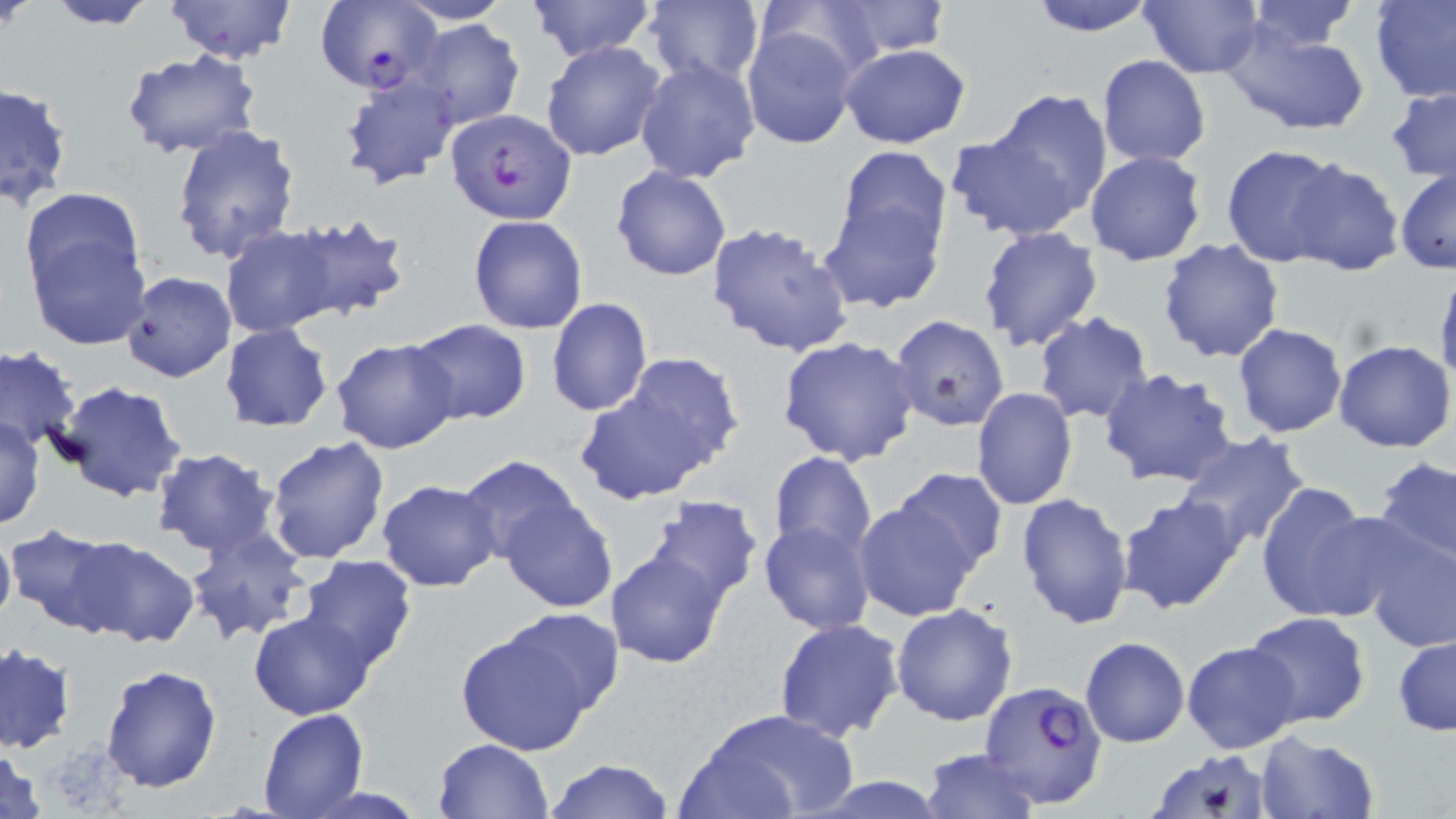 Approximate bounding boxes as named x1/y1/x2/y2 corners in pixels. Uninfected red blood cell locations: (x1=163, y1=0, x2=296, y2=64), (x1=526, y1=0, x2=657, y2=64), (x1=755, y1=0, x2=888, y2=83), (x1=1027, y1=0, x2=1159, y2=37), (x1=1136, y1=0, x2=1263, y2=78), (x1=1369, y1=0, x2=1456, y2=103), (x1=41, y1=1, x2=159, y2=29), (x1=394, y1=1, x2=514, y2=24), (x1=642, y1=1, x2=764, y2=85), (x1=825, y1=1, x2=952, y2=58), (x1=1244, y1=1, x2=1363, y2=53), (x1=406, y1=18, x2=526, y2=132), (x1=1223, y1=20, x2=1371, y2=138), (x1=741, y1=24, x2=860, y2=149), (x1=540, y1=40, x2=668, y2=161), (x1=839, y1=43, x2=971, y2=148), (x1=120, y1=50, x2=266, y2=161), (x1=1097, y1=55, x2=1210, y2=167), (x1=634, y1=56, x2=761, y2=184), (x1=337, y1=70, x2=460, y2=191), (x1=0, y1=83, x2=72, y2=209), (x1=1385, y1=86, x2=1456, y2=185), (x1=981, y1=90, x2=1113, y2=224), (x1=170, y1=124, x2=301, y2=263), (x1=944, y1=130, x2=1090, y2=241), (x1=1220, y1=143, x2=1346, y2=266), (x1=832, y1=147, x2=952, y2=260), (x1=1084, y1=149, x2=1207, y2=267), (x1=1282, y1=158, x2=1404, y2=276), (x1=610, y1=167, x2=731, y2=281), (x1=1395, y1=169, x2=1455, y2=274), (x1=816, y1=193, x2=948, y2=314), (x1=19, y1=201, x2=151, y2=348), (x1=281, y1=212, x2=409, y2=322), (x1=467, y1=214, x2=590, y2=334), (x1=708, y1=220, x2=856, y2=357), (x1=221, y1=225, x2=339, y2=338), (x1=977, y1=226, x2=1105, y2=351), (x1=1156, y1=237, x2=1285, y2=363), (x1=1434, y1=266, x2=1456, y2=388), (x1=120, y1=272, x2=235, y2=384), (x1=545, y1=297, x2=653, y2=418), (x1=1032, y1=311, x2=1155, y2=425), (x1=889, y1=314, x2=1010, y2=430), (x1=404, y1=319, x2=531, y2=425), (x1=220, y1=323, x2=333, y2=432), (x1=1232, y1=323, x2=1346, y2=437), (x1=777, y1=336, x2=921, y2=466), (x1=330, y1=338, x2=460, y2=455), (x1=1333, y1=340, x2=1455, y2=452), (x1=0, y1=345, x2=82, y2=453), (x1=625, y1=353, x2=745, y2=469), (x1=1099, y1=366, x2=1240, y2=488), (x1=574, y1=370, x2=729, y2=504), (x1=53, y1=381, x2=188, y2=503), (x1=972, y1=388, x2=1077, y2=510), (x1=0, y1=417, x2=45, y2=531), (x1=1173, y1=432, x2=1313, y2=550), (x1=265, y1=435, x2=391, y2=565), (x1=151, y1=448, x2=279, y2=558), (x1=767, y1=450, x2=877, y2=564), (x1=456, y1=456, x2=585, y2=569), (x1=1371, y1=456, x2=1456, y2=568), (x1=887, y1=468, x2=1009, y2=575), (x1=376, y1=479, x2=502, y2=593), (x1=1255, y1=482, x2=1381, y2=623), (x1=852, y1=491, x2=984, y2=622), (x1=1015, y1=492, x2=1134, y2=630), (x1=1116, y1=493, x2=1246, y2=615), (x1=495, y1=494, x2=619, y2=612), (x1=640, y1=495, x2=764, y2=608), (x1=758, y1=521, x2=876, y2=635), (x1=0, y1=522, x2=16, y2=640), (x1=184, y1=524, x2=313, y2=643), (x1=5, y1=526, x2=122, y2=633), (x1=1358, y1=529, x2=1456, y2=654), (x1=66, y1=534, x2=198, y2=646), (x1=606, y1=545, x2=731, y2=671), (x1=296, y1=557, x2=418, y2=673), (x1=891, y1=602, x2=1019, y2=725), (x1=249, y1=610, x2=376, y2=719), (x1=1241, y1=611, x2=1371, y2=730), (x1=453, y1=612, x2=613, y2=753), (x1=774, y1=618, x2=905, y2=741), (x1=1392, y1=634, x2=1455, y2=737), (x1=1080, y1=636, x2=1190, y2=748), (x1=1181, y1=641, x2=1304, y2=754), (x1=0, y1=643, x2=75, y2=755), (x1=101, y1=664, x2=222, y2=793), (x1=257, y1=709, x2=370, y2=819), (x1=697, y1=709, x2=858, y2=818), (x1=1254, y1=732, x2=1380, y2=819), (x1=433, y1=738, x2=554, y2=819), (x1=0, y1=743, x2=49, y2=819), (x1=920, y1=748, x2=1039, y2=818), (x1=1149, y1=749, x2=1274, y2=819), (x1=543, y1=759, x2=677, y2=818). Plasmodium falciparum-infected red blood cell locations: (x1=315, y1=0, x2=438, y2=96), (x1=443, y1=108, x2=578, y2=225), (x1=978, y1=680, x2=1110, y2=809). Slide-level diagnosis: Plasmodium falciparum. Captured at 1000x magnification. Optical microscopy. Image is 1456×819 pixels. May-Grünwald-Giemsa stain. Single field of view. Thin blood film.